Name the parasite shown.
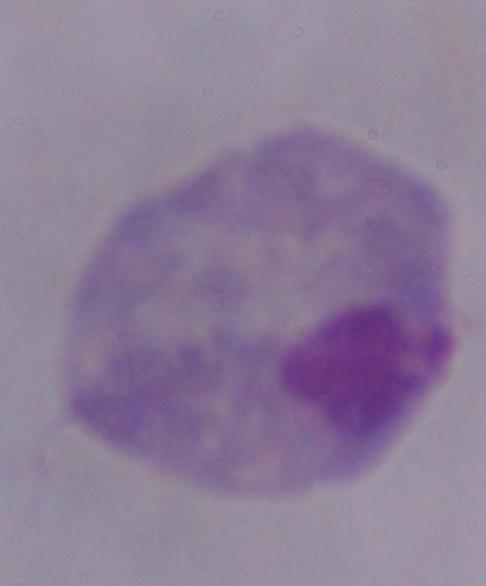

A trichomonad.

Summary:
  - Magnification: 1000x
  - Modality: micrograph